Name the parasite shown.
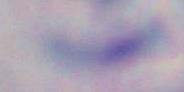
Toxoplasma gondii.

magnification = 1000x
modality = micrograph